Give the preparation type.
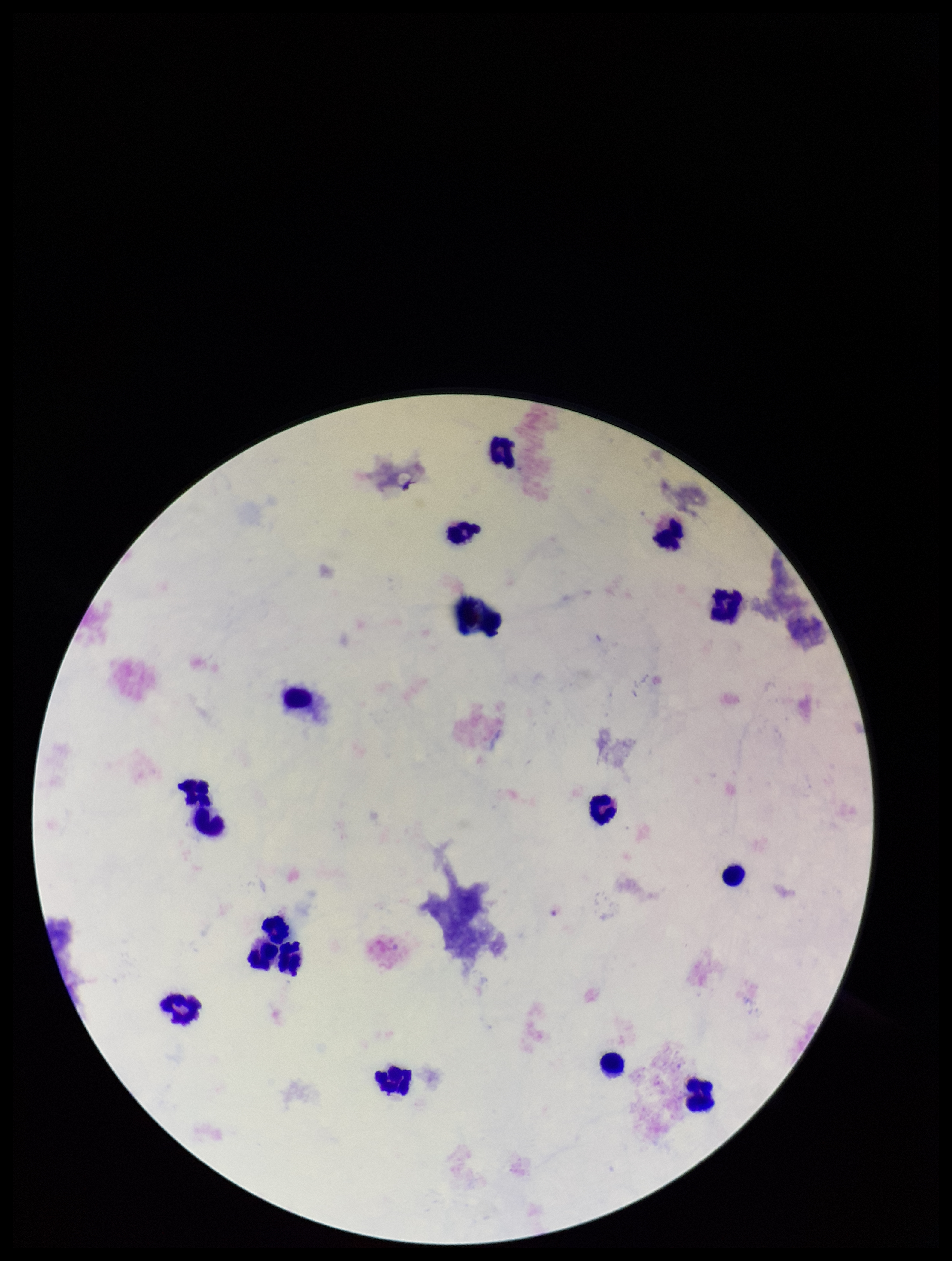

It is a thick blood smear.

Summary:
  - Capture: smartphone photograph through the microscope eyepiece
  - Leukocyte count: 17
  - Stain: Giemsa
  - Image size: 952×1261 pixels
  - Plasmodium parasites: none seen
  - Field of view: single
  - Parasite count: 0
  - Patient malaria status: negative